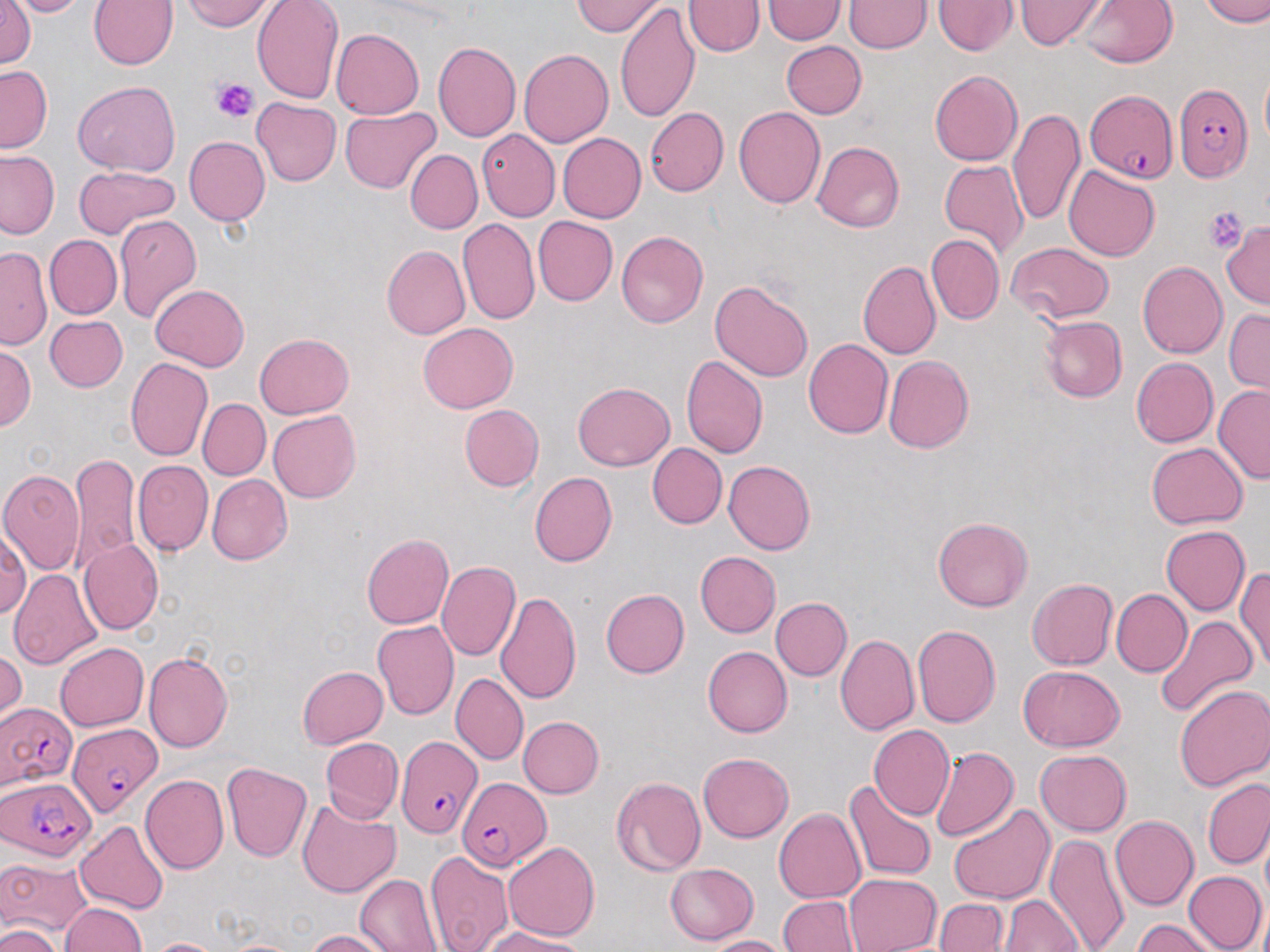 Approximate bounding boxes as [x1, y1, x2, y2] in pixels. Uninfected red blood cell locations: [1, 0, 35, 70], [4, 0, 95, 17], [179, 0, 277, 32], [251, 0, 343, 103], [1077, 0, 1179, 67], [1201, 0, 1270, 27], [89, 1, 178, 70], [573, 1, 667, 36], [684, 1, 764, 57], [762, 1, 846, 44], [843, 1, 931, 53], [932, 1, 1018, 56], [1014, 1, 1109, 49], [615, 3, 700, 125], [331, 29, 424, 120], [781, 40, 867, 118], [433, 42, 522, 142], [519, 49, 613, 148], [0, 65, 51, 152], [929, 70, 1022, 167], [1261, 70, 1270, 149], [73, 82, 179, 176], [252, 98, 341, 187], [734, 106, 826, 208], [1008, 106, 1084, 226], [340, 107, 440, 193], [645, 108, 728, 196], [476, 129, 560, 222], [548, 133, 634, 304], [558, 133, 647, 223], [184, 136, 270, 225], [812, 141, 905, 232], [405, 149, 482, 235], [0, 150, 59, 239], [940, 159, 1029, 259], [73, 165, 180, 239], [1065, 165, 1160, 261], [114, 213, 202, 322], [533, 215, 617, 306], [457, 218, 539, 326], [1220, 221, 1270, 310], [616, 231, 709, 328], [926, 234, 1003, 325], [45, 235, 122, 319], [1007, 242, 1114, 324], [381, 245, 470, 339], [0, 246, 52, 349], [859, 259, 941, 360], [1137, 261, 1228, 359], [710, 279, 813, 383], [150, 284, 249, 372], [1224, 308, 1269, 396], [45, 315, 127, 391], [1038, 315, 1126, 403], [419, 323, 518, 413], [254, 333, 355, 419], [803, 338, 893, 439], [0, 344, 36, 431], [681, 355, 768, 459], [883, 355, 975, 453], [125, 356, 212, 461], [1131, 357, 1219, 447], [572, 381, 673, 470], [1213, 385, 1270, 485], [197, 399, 270, 480], [460, 404, 544, 491], [268, 410, 361, 503], [1146, 442, 1247, 528], [647, 443, 727, 528], [69, 451, 141, 572], [133, 460, 212, 556], [723, 460, 815, 555], [0, 468, 85, 573], [530, 472, 617, 567], [207, 474, 292, 565], [932, 517, 1032, 612], [0, 524, 30, 623], [1161, 526, 1251, 615], [361, 533, 454, 629], [78, 539, 163, 635], [695, 551, 781, 637], [436, 562, 522, 661], [1235, 565, 1270, 672], [9, 568, 103, 670], [1027, 578, 1118, 670], [601, 588, 689, 678], [1112, 589, 1192, 676], [495, 590, 582, 704], [771, 597, 852, 680], [1153, 616, 1259, 719], [373, 620, 459, 720], [912, 624, 1001, 728], [836, 634, 919, 736], [55, 643, 148, 731], [703, 646, 793, 737], [0, 648, 25, 730], [144, 652, 233, 752], [1018, 665, 1125, 752], [297, 666, 388, 748], [450, 672, 527, 765], [1173, 683, 1270, 792], [517, 716, 604, 798], [869, 725, 955, 820], [321, 737, 404, 822], [930, 747, 1018, 843], [1036, 750, 1131, 836], [698, 752, 793, 842], [222, 763, 314, 863], [139, 775, 229, 875], [610, 777, 706, 877], [1203, 778, 1270, 869], [844, 780, 936, 880], [296, 798, 400, 898], [948, 802, 1055, 906], [774, 807, 866, 903], [1110, 815, 1198, 910], [76, 820, 168, 915], [1045, 834, 1130, 952], [502, 842, 600, 942], [425, 850, 514, 952], [0, 855, 91, 938], [665, 863, 759, 945], [1183, 871, 1267, 952], [355, 873, 443, 951], [844, 873, 942, 952], [999, 895, 1083, 951], [777, 896, 860, 951], [933, 899, 1009, 951], [59, 903, 147, 952], [1134, 919, 1220, 952], [2, 924, 62, 952], [479, 927, 589, 951], [303, 929, 394, 951], [705, 935, 790, 952], [142, 938, 229, 952]. Plasmodium falciparum-infected red blood cell locations: [1174, 83, 1252, 181], [1084, 89, 1179, 182], [1, 701, 77, 790], [68, 722, 161, 817], [396, 730, 479, 838], [457, 775, 551, 870], [1, 777, 96, 862]. Platelet locations: [210, 77, 258, 123], [1203, 206, 1249, 253]. Slide-level diagnosis: Plasmodium falciparum. Light microscopy. One field of a larger specimen. Image is 1270×952 pixels. Captured at 1000x magnification. May-Grünwald-Giemsa-stained preparation. Thin blood smear.